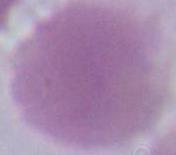
{
  "identification": "red blood cell",
  "modality": "photomicrograph",
  "magnification": "1000x"
}